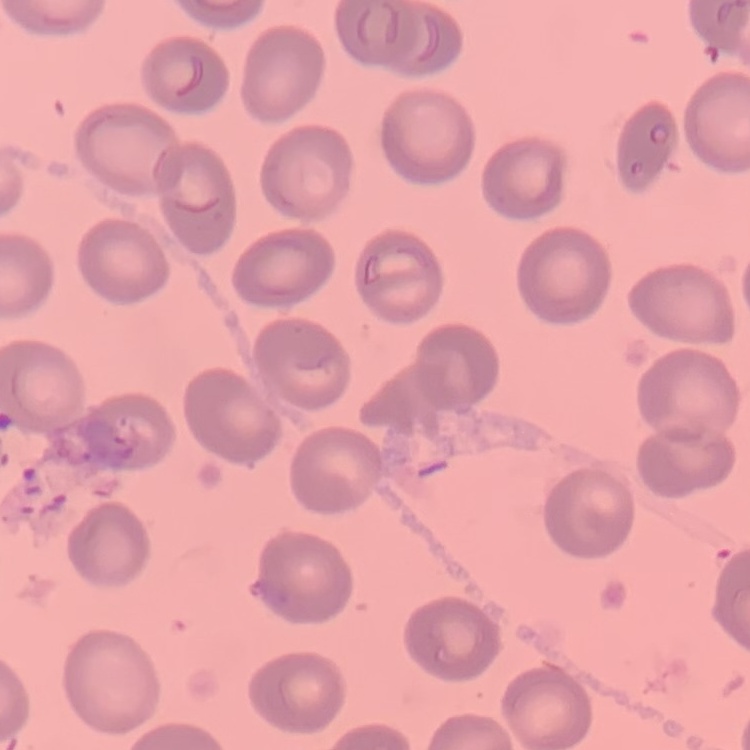

{
  "erythrocyte_morphology": "no rouleaux formation",
  "preparation": "thin blood film",
  "stain": "Field's or Giemsa",
  "image_type": "square crop of a larger photomicrograph"
}